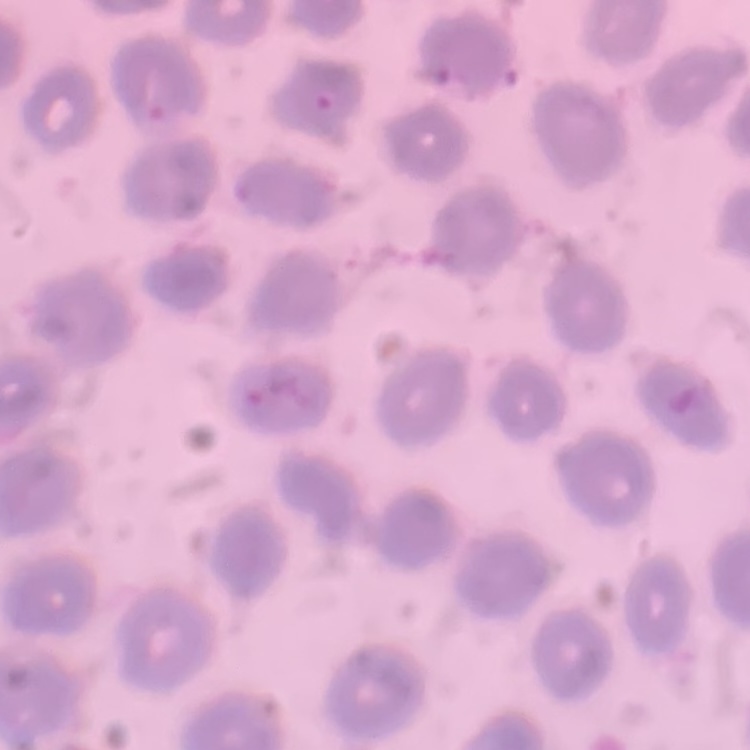

Summary:
  - Red blood cell morphology: no rouleaux formation
  - Preparation: thin blood film
  - Stain: Field's or Giemsa
  - Image type: one tile cut from a larger photomicrograph